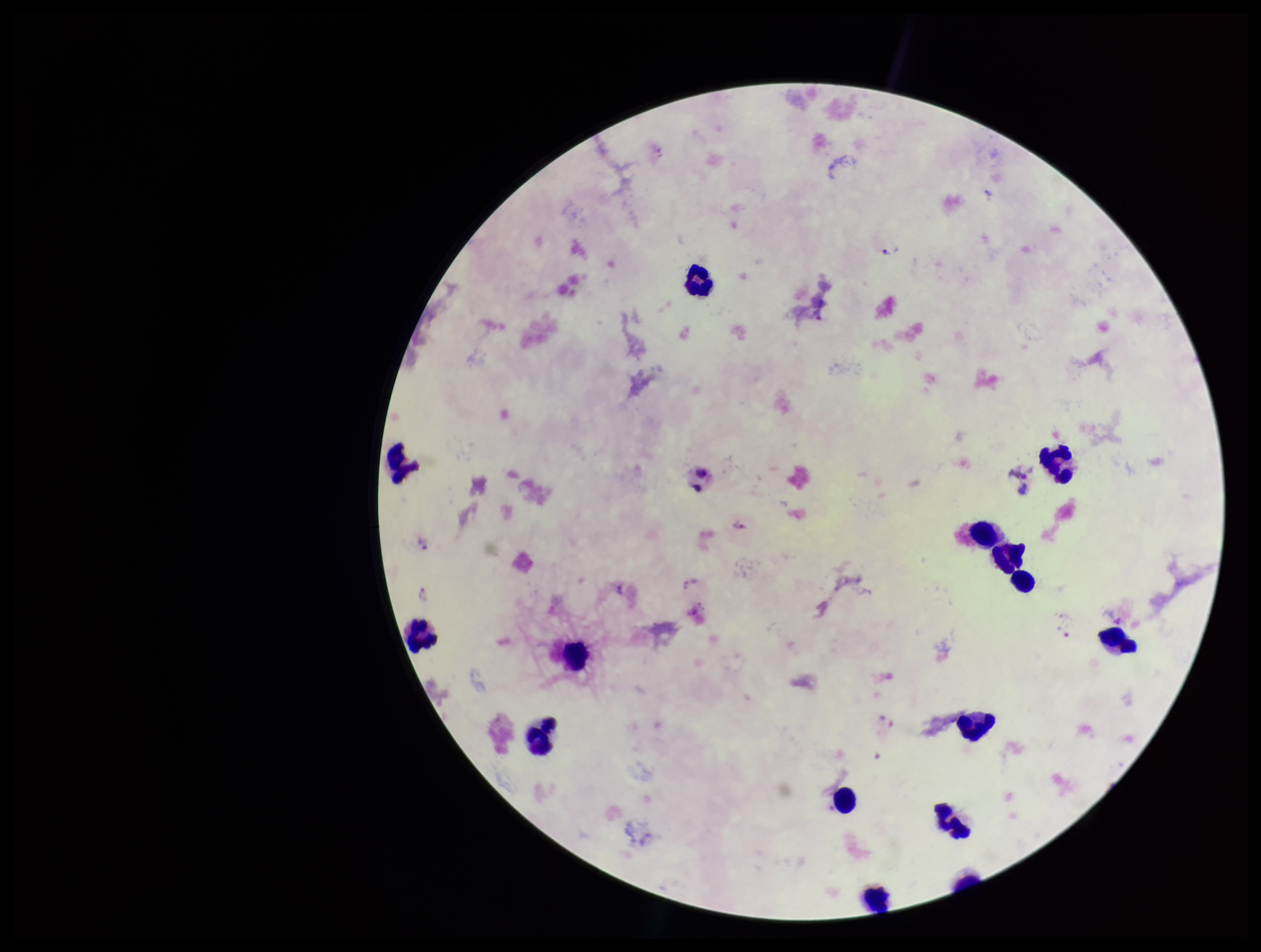
Parasite count: 0. One field from this slide. Patient malaria status: positive. Species reported for this patient: Plasmodium vivax. Leukocyte count: 15. Preparation: thick. Giemsa stain. Plasmodium parasites: none identified. Image is 1261×952 pixels. Photographed through the microscope eyepiece with a smartphone camera.